Report the malaria status of this cell.
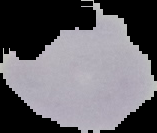
Parasitized.

Summary:
  - Preparation: thin blood smear
  - Image size: 157×133 pixels
  - Image type: cell region segmented out of the field of view; surrounding area masked to black